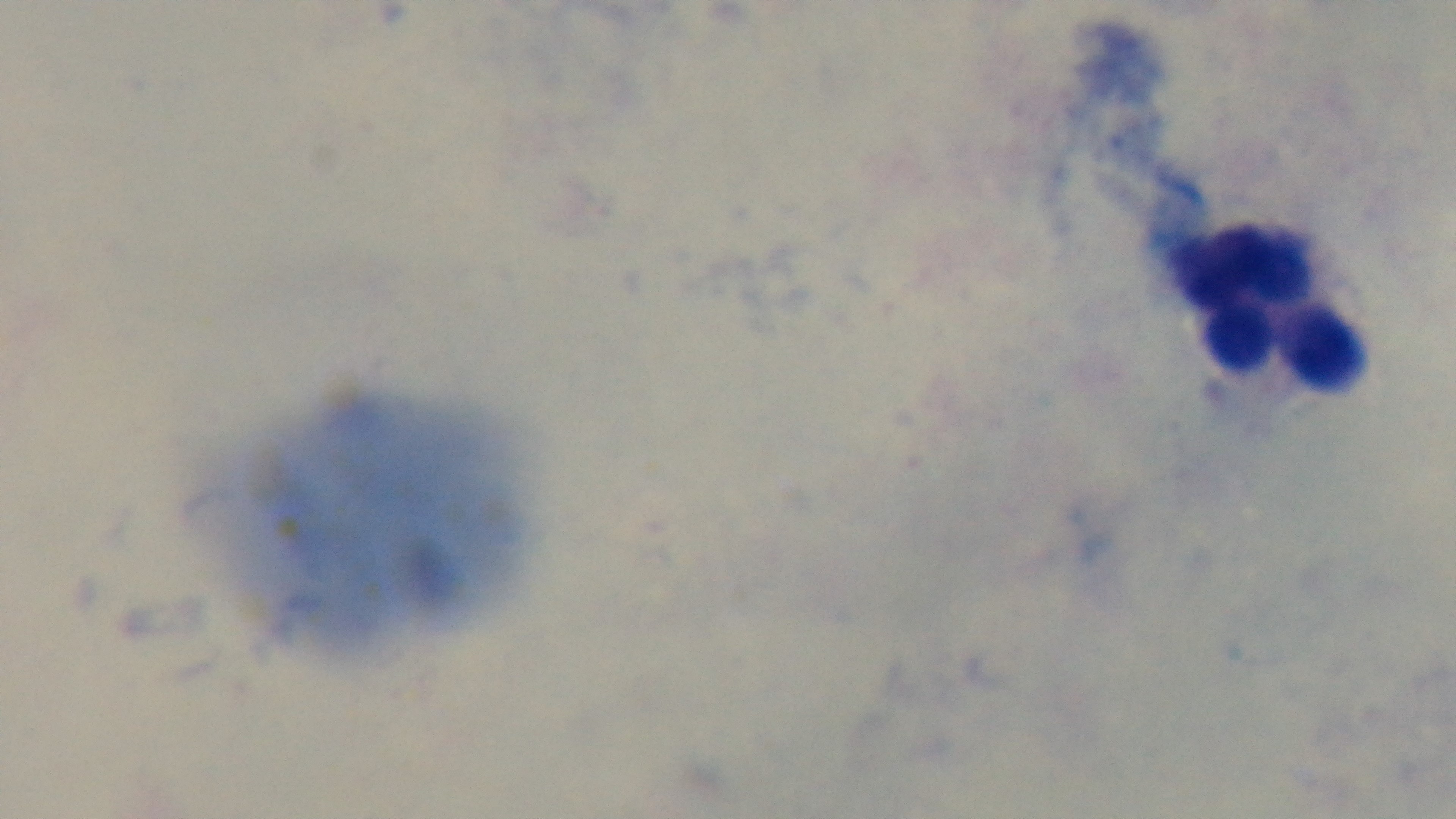 Giemsa stain. Light microscopy. Preparation: thick smear. Malaria status: negative. Oil-immersion objective, 100x. Captured with a mounted 4K digital camera. Single field of view.